Outline each Trypanosoma brucei.
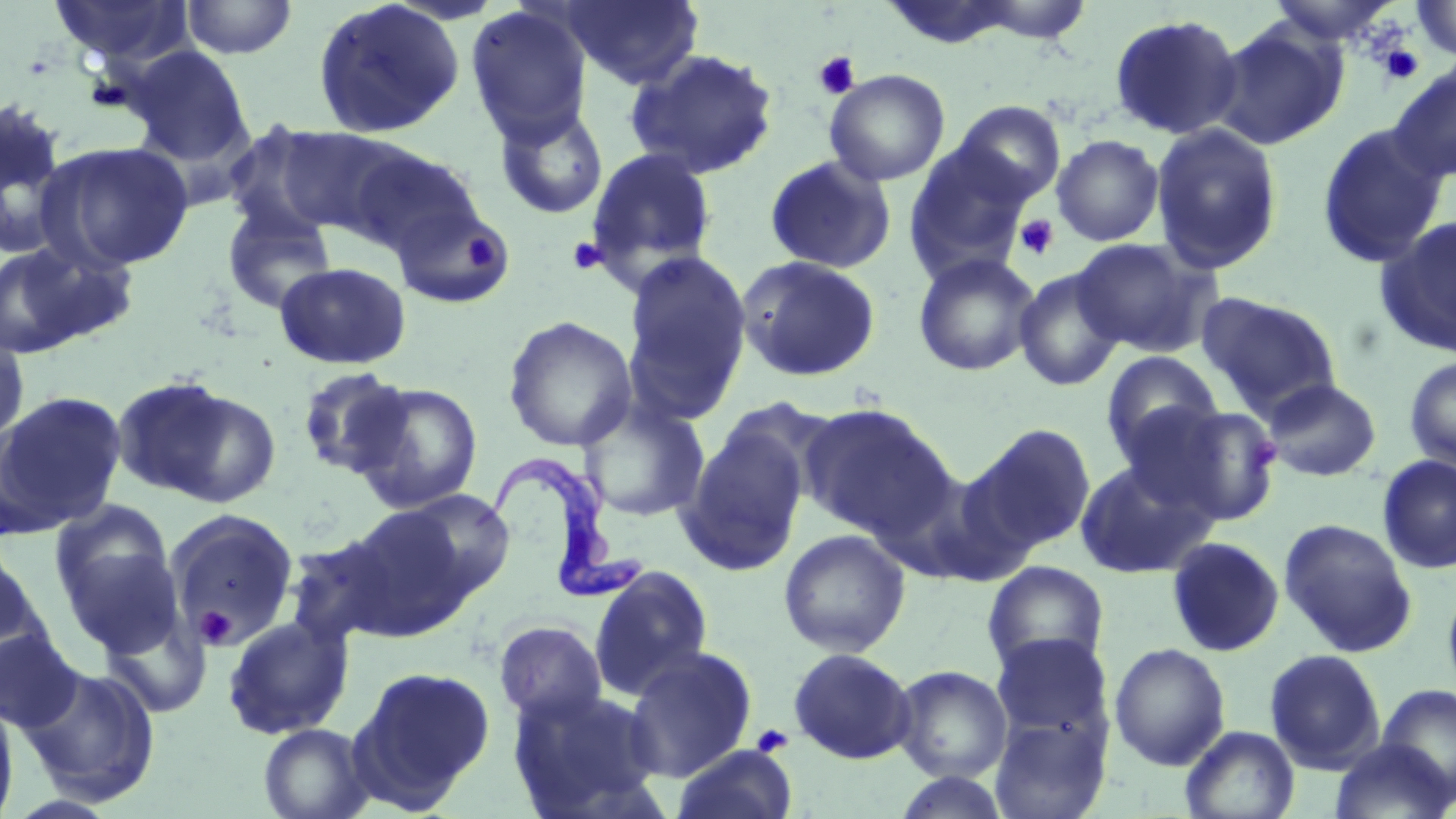
Approximate bounding boxes as (x1,y1)-(x2,y2) corner pairs in pixels.
Trypanosoma brucei: (475,461)-(645,603).

Uninfected red blood cell locations: (48,0)-(195,69), (180,0)-(298,59), (312,0)-(465,139), (562,0)-(702,89), (971,0)-(1092,44), (1264,0)-(1401,47), (1413,0)-(1456,61), (880,1)-(1022,50), (466,4)-(593,142), (1108,13)-(1244,141), (1211,22)-(1348,149), (125,45)-(252,165), (624,47)-(780,180), (1388,63)-(1456,182), (824,69)-(950,186), (0,99)-(73,259), (952,101)-(1066,205), (492,103)-(609,220), (221,121)-(346,242), (1149,122)-(1284,274), (1315,123)-(1449,269), (275,126)-(413,237), (1051,134)-(1164,246), (37,140)-(196,271), (904,141)-(1036,279), (345,146)-(485,258), (583,147)-(719,285), (764,155)-(897,274), (221,200)-(337,315), (392,200)-(514,309), (1375,217)-(1456,357), (1071,237)-(1220,357), (0,244)-(100,358), (622,251)-(752,415), (912,252)-(1041,377), (736,256)-(881,382), (274,261)-(411,369), (1014,268)-(1124,391), (1196,292)-(1341,416), (502,316)-(638,452), (0,330)-(31,449), (1100,351)-(1224,458), (1403,356)-(1456,473), (295,366)-(413,479), (111,376)-(267,507), (1262,378)-(1381,481), (350,381)-(483,513), (0,391)-(126,535), (578,398)-(710,523), (800,403)-(954,539), (1147,405)-(1283,526), (969,423)-(1096,554), (677,426)-(809,577), (1376,454)-(1456,574), (1074,459)-(1217,580), (395,488)-(516,600), (49,503)-(182,653), (340,505)-(476,638), (163,509)-(300,650), (1278,517)-(1417,657), (778,529)-(910,657), (281,534)-(404,649), (1165,536)-(1285,657), (1,539)-(49,678), (982,561)-(1109,676), (588,565)-(713,699), (1442,579)-(1456,701), (100,609)-(211,719), (221,615)-(354,739), (493,619)-(609,726), (0,627)-(84,734), (991,633)-(1112,742), (1109,642)-(1231,771), (623,646)-(758,782), (788,648)-(916,764), (1264,648)-(1385,772), (17,663)-(162,806), (892,665)-(1013,783), (350,666)-(495,810), (1376,684)-(1456,801), (509,687)-(665,818), (0,696)-(19,819), (990,713)-(1110,819), (258,722)-(373,819), (1181,726)-(1300,819), (1329,738)-(1454,819), (672,744)-(797,819), (891,771)-(1011,818). Platelet locations: (1414,0)-(1456,59), (1376,42)-(1425,85), (812,51)-(861,99), (1013,214)-(1060,261), (464,228)-(504,270), (568,238)-(608,276), (193,607)-(237,651), (750,723)-(794,758). Slide-level diagnosis: Trypanosoma brucei. May-Grünwald-Giemsa stain. Optical microscopy. One field of a larger specimen. 1000x magnification. Image is 1456×819 pixels. Thin blood film.